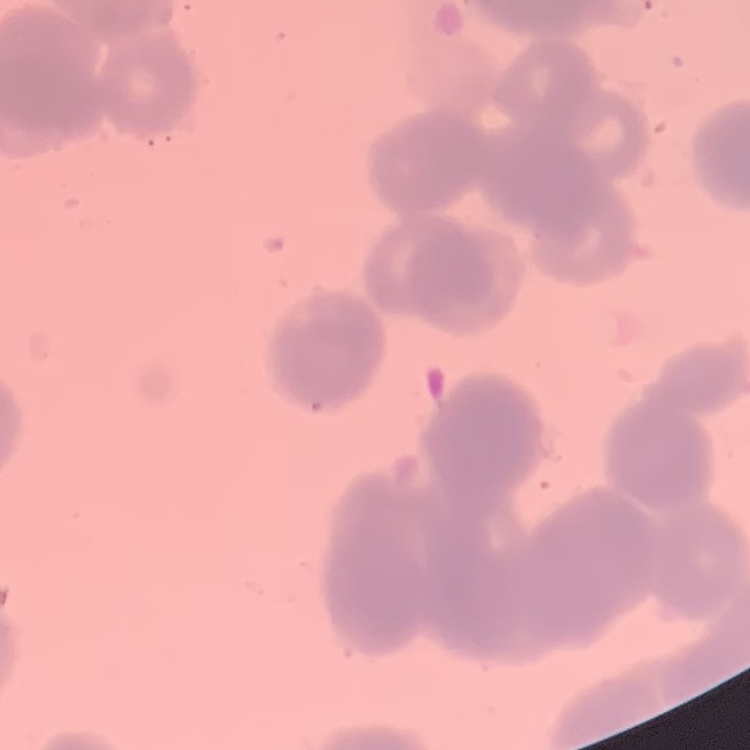

{
  "red_blood_cell_morphology": "rouleaux formation",
  "stain": "Field's or Giemsa",
  "preparation": "thin blood smear",
  "image_type": "square crop of a larger photomicrograph"
}